Point out each leukocyte.
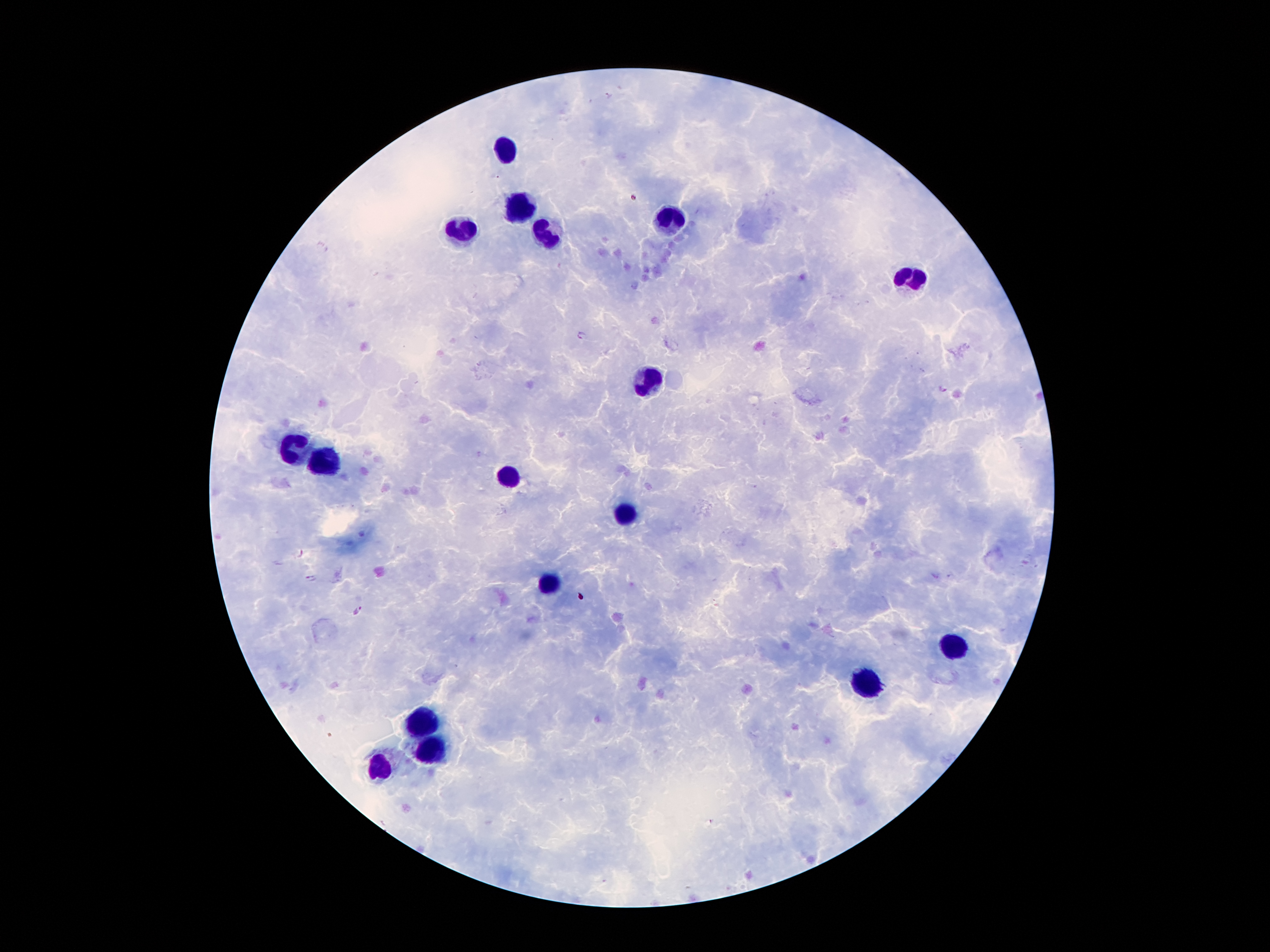

Approximate centers as (x, y) in pixels.
Leukocytes: (506, 150), (521, 208), (674, 219), (461, 228), (548, 237), (917, 274), (649, 380), (289, 447), (329, 464), (510, 477), (630, 515), (548, 584), (957, 648), (866, 683), (424, 721), (431, 749), (380, 767).

Plasmodium parasite locations: (583, 336), (942, 388), (301, 553), (311, 579), (358, 609). Image is 1270×952 pixels. Photographed through the microscope eyepiece with a smartphone camera. 100x magnification. Giemsa-stained preparation. Single field of view. Thick blood film. Patient malaria status: infected with Plasmodium falciparum.